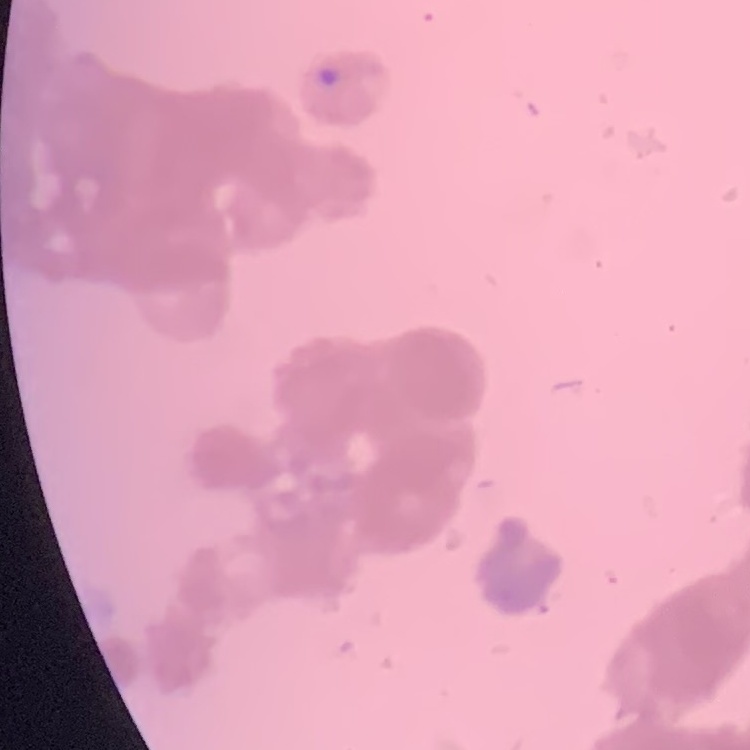
The erythrocytes exhibit rouleaux formation. Thin blood smear. Field's or Giemsa stain. Square crop of a larger photomicrograph.